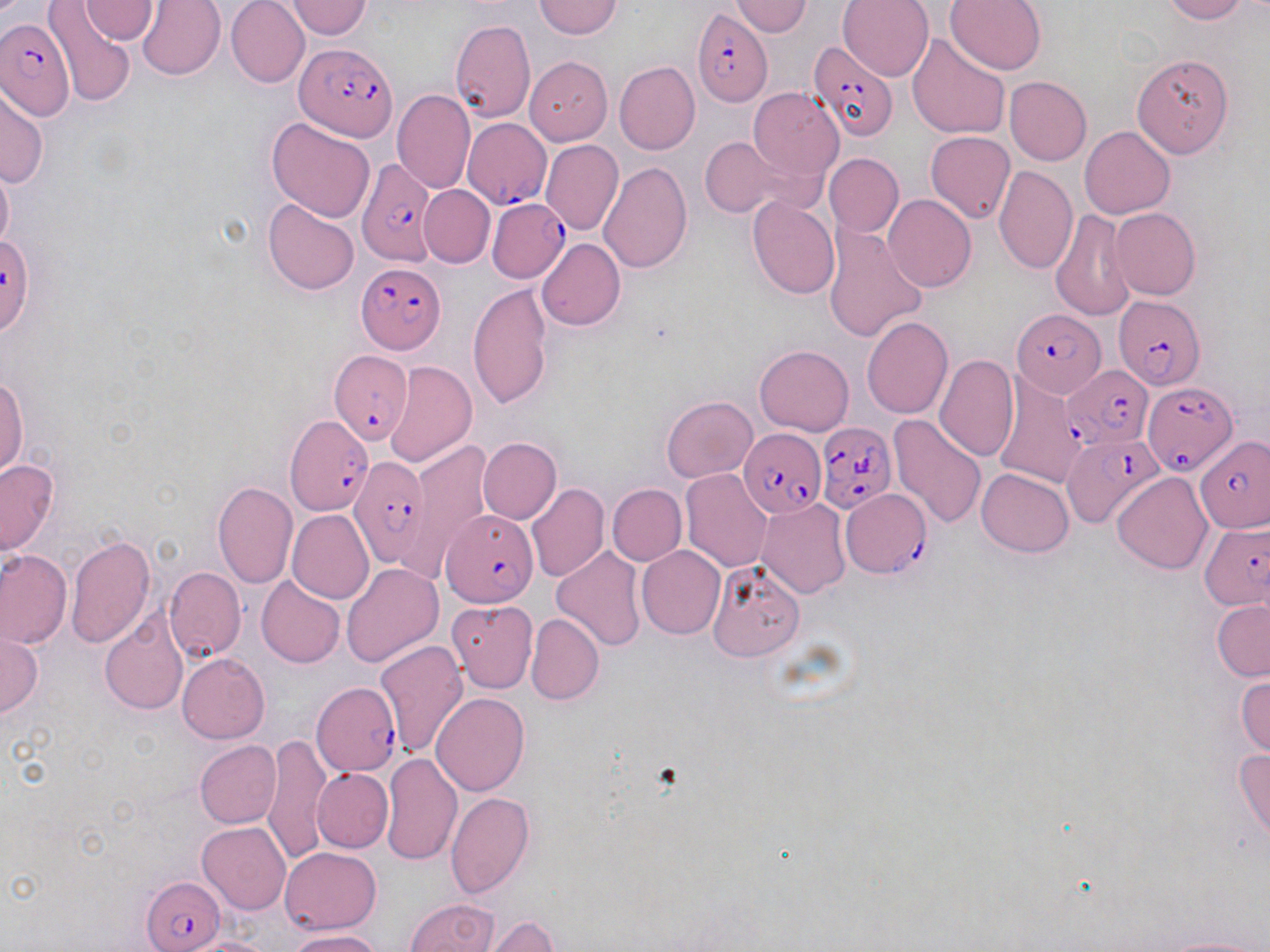
slide_level_diagnosis: Plasmodium falciparum
field_of_view: one of a larger specimen
image_size: 1270×952 pixels
modality: light microscopy
magnification: 1000x
stain: May-Grünwald-Giemsa
preparation: thin blood film
uninfected_red_blood_cell_locations: 'approximate bounding boxes as [x1, y1, x2, y2] in pixels: [136, 0, 226, 81], [226, 0, 309, 88], [534, 0, 621, 39], [838, 0, 933, 82], [945, 0, 1046, 75], [1160, 0, 1246, 23], [78, 1, 159, 43], [285, 1, 373, 39], [728, 1, 813, 36], [44, 3, 137, 106], [449, 21, 536, 123], [907, 34, 1010, 140], [1131, 52, 1233, 159], [525, 56, 612, 145], [613, 61, 699, 156], [1005, 77, 1091, 165], [749, 86, 844, 181], [0, 87, 48, 188], [392, 89, 474, 193], [266, 116, 376, 223], [1080, 126, 1175, 218], [925, 130, 1015, 223], [700, 136, 793, 217], [541, 140, 623, 235], [824, 153, 903, 236], [0, 161, 14, 252], [598, 162, 693, 273], [995, 165, 1078, 274], [418, 186, 494, 268], [884, 195, 976, 291], [747, 197, 840, 299], [264, 198, 360, 295], [1109, 208, 1201, 299], [1050, 210, 1135, 322], [823, 223, 927, 343], [536, 238, 625, 330], [468, 282, 554, 411], [862, 316, 953, 419], [755, 344, 854, 436], [934, 355, 1019, 461], [385, 361, 476, 467], [0, 375, 29, 477], [994, 377, 1089, 487], [662, 397, 756, 481], [889, 413, 988, 528], [478, 437, 561, 524], [406, 439, 491, 570], [0, 458, 59, 557], [976, 467, 1074, 557], [681, 468, 772, 572], [1112, 472, 1213, 574], [211, 481, 298, 589], [525, 482, 609, 582], [607, 484, 686, 566], [755, 498, 851, 599], [287, 509, 374, 604], [529, 510, 627, 624], [66, 534, 156, 648], [552, 545, 646, 651], [636, 545, 726, 639], [1, 548, 71, 649], [341, 562, 443, 667], [707, 562, 804, 662], [164, 565, 246, 662], [256, 576, 344, 668], [1212, 598, 1270, 681], [447, 600, 538, 693], [100, 613, 187, 716], [526, 614, 603, 705], [0, 629, 41, 719], [374, 639, 469, 760], [177, 653, 269, 744], [1235, 672, 1270, 759], [432, 692, 529, 795], [262, 733, 332, 863], [194, 740, 282, 828], [1234, 747, 1270, 845], [380, 751, 462, 865], [312, 768, 394, 852], [445, 793, 535, 898], [197, 822, 291, 914], [279, 847, 381, 934], [405, 897, 500, 952], [477, 915, 560, 952], [289, 929, 384, 952], [1153, 935, 1270, 952], [184, 937, 280, 952]'
plasmodium_falciparum_infected_red_blood_cell_locations: 'approximate bounding boxes as [x1, y1, x2, y2] in pixels: [691, 8, 774, 107], [1, 20, 73, 120], [807, 41, 897, 144], [297, 42, 397, 140], [463, 119, 550, 208], [352, 158, 445, 262], [489, 199, 569, 281], [1, 232, 36, 336], [357, 263, 443, 353], [1113, 291, 1205, 390], [1013, 309, 1105, 399], [328, 349, 411, 447], [1063, 365, 1154, 449], [1143, 378, 1238, 478], [285, 413, 376, 516], [815, 422, 896, 513], [739, 427, 826, 518], [1063, 430, 1163, 528], [1195, 436, 1268, 532], [349, 454, 430, 566], [840, 489, 928, 576], [441, 509, 536, 606], [1199, 522, 1270, 610], [312, 682, 400, 777], [143, 877, 225, 951]'